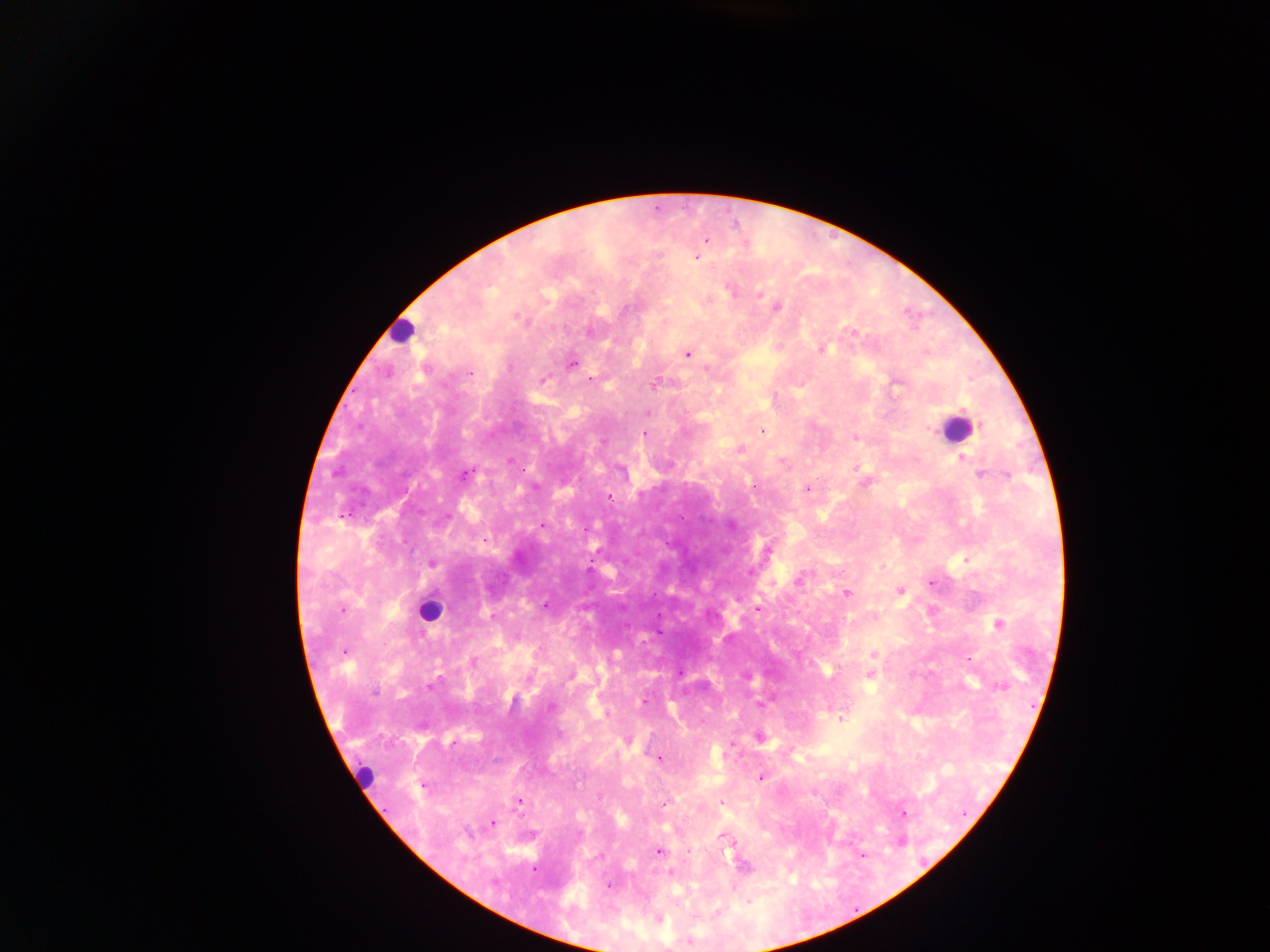

leukocyte locations = approximate centers as x y in pixels: 402 331; 956 428; 428 611; 364 772
preparation = thick blood smear
country = Ghana
capture = mobile-phone photograph through a microscope
Plasmodium parasite locations = approximate centers as x y in pixels: 707 240; 697 257; 731 290; 760 294; 767 301; 777 307; 624 309; 590 332; 853 333; 822 349; 688 354; 572 364; 706 368; 470 372; 590 379; 543 380; 654 384; 896 385; 648 413; 763 431; 644 434; 855 437; 962 458; 510 461; 856 468; 464 474; 980 474; 1006 475; 754 485; 807 489; 609 498; 542 525; 484 540; 768 549; 966 560; 433 564; 750 571; 799 579; 931 582; 900 591; 846 593; 545 605; 342 610; 757 610; 491 616; 998 624; 344 651; 873 654; 681 673; 870 675; 430 687; 375 692; 644 700; 761 704; 550 707; 841 719; 759 737; 453 742; 659 759; 760 777; 424 786; 664 802; 721 802; 518 803; 903 814; 492 823; 725 839; 659 851; 600 856; 534 870; 671 873; 609 885; 658 919
image size = 1270×952 pixels
field of view = single